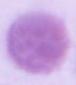

identification = erythrocyte
modality = micrograph
magnification = 1000x